Classify this cell by malaria status.
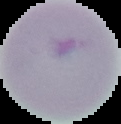

Uninfected.

image size = 121×124 pixels
image type = segmented cell region with the area outside set to black
preparation = thin blood film